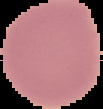
{
  "image_size": "103×109 pixels",
  "preparation": "thin blood film",
  "image_type": "segmented cell region on a black background",
  "malaria_status": "uninfected"
}